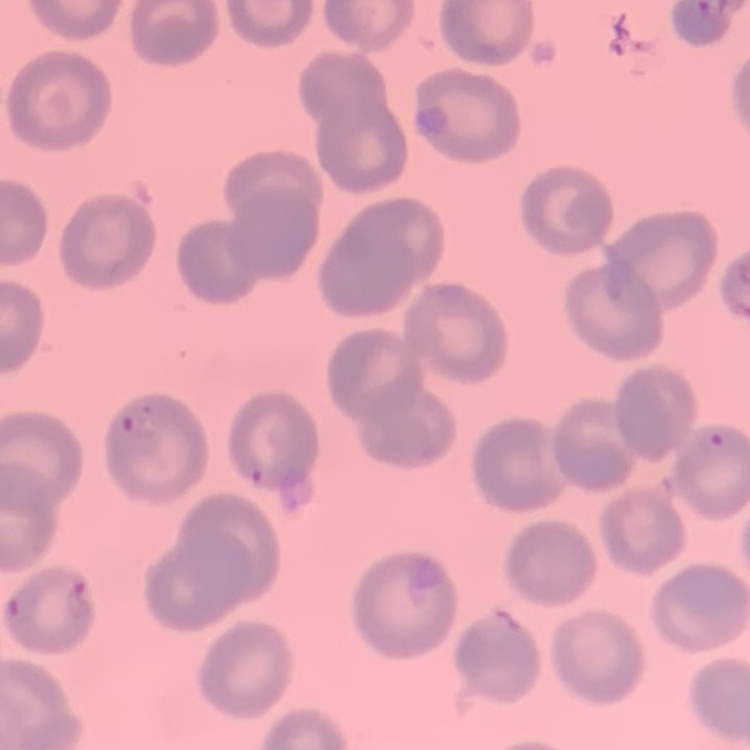
Summary:
  - Red blood cell morphology: no rouleaux formation
  - Image type: one tile cut from a larger photomicrograph
  - Preparation: thin blood film
  - Stain: Field's or Giemsa